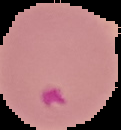 Segmented cell region on a black background. Image is 121×130 pixels. Malaria status: parasitized. From a thin blood film.